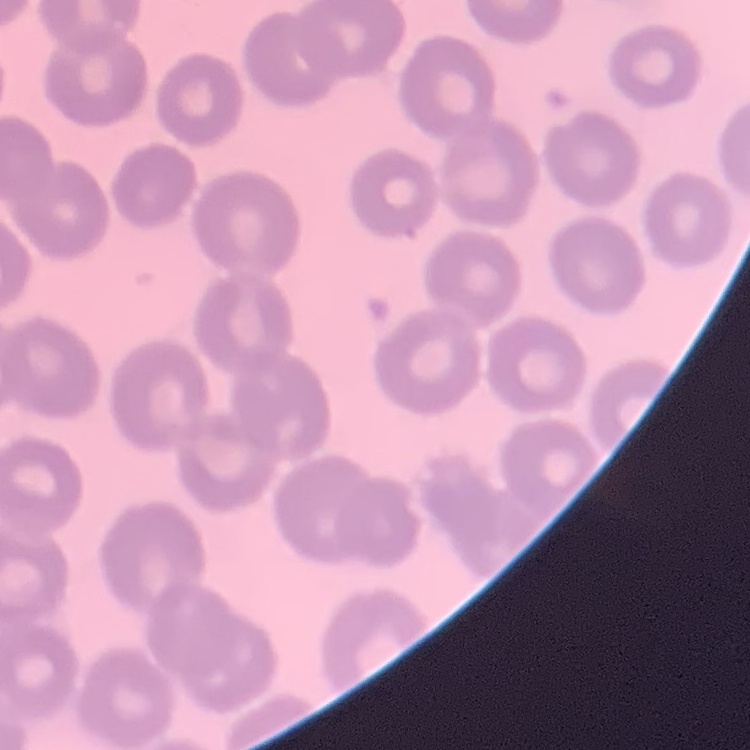 The erythrocytes show no rouleaux formation. One tile cut from a larger photomicrograph. Thin blood smear. Stained with either Field's or Giemsa.